Mark where leukocytes are.
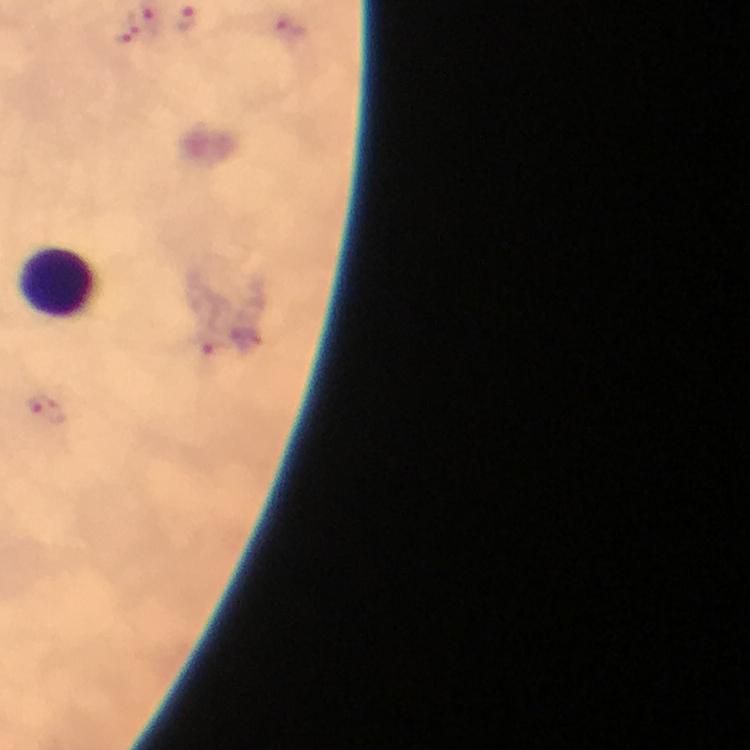

Approximate centers as [x, y] in pixels.
Leukocytes: [63, 283].

Malaria parasite locations: [186, 22], [127, 29], [287, 32], [208, 346], [48, 412]. 100x magnification. Thick blood film. Smartphone photograph taken through a microscope. A crop from one field of view. Image is 750×750 pixels. Giemsa stain. Immersion oil applied. From a malaria diagnostic workup.